Name the parasite shown.
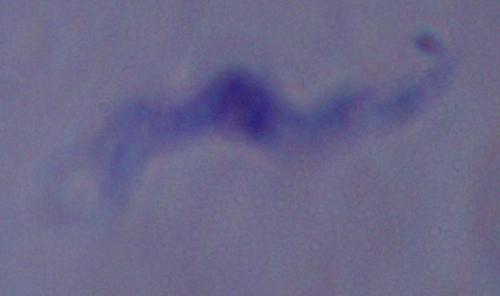

A trypanosome.

modality = photomicrograph
magnification = 1000x